Assess this cell for malaria.
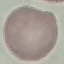

Uninfected.

Giemsa-stained preparation. Photographed with a smartphone camera at the microscope eyepiece. Cell patch, automatically extracted from a larger field of view and resized to 64 × 64 pixels. Thin smear of blood.